Classify this cell by malaria status.
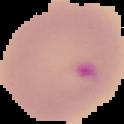
Parasitized.

{
  "image_type": "cell region segmented out of the field of view; surrounding area masked to black",
  "preparation": "thin blood smear",
  "image_size": "124×124 pixels"
}